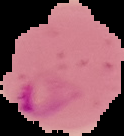

Image is 124×136 pixels. Result: malaria parasites identified. From a thin blood smear. The area outside the segmented cell region is set to black.